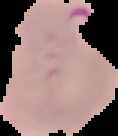
result = malaria parasites identified
image size = 118×136 pixels
preparation = thin blood film
image type = segmented cell region with the area outside set to black